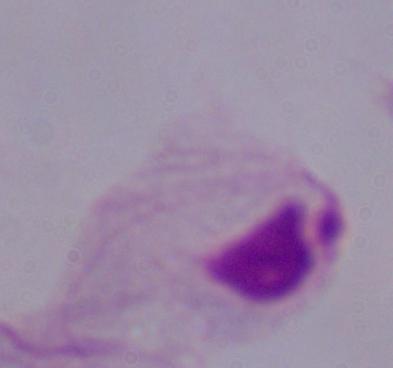

{
  "magnification": "1000x",
  "modality": "micrograph",
  "identification": "trichomonad"
}